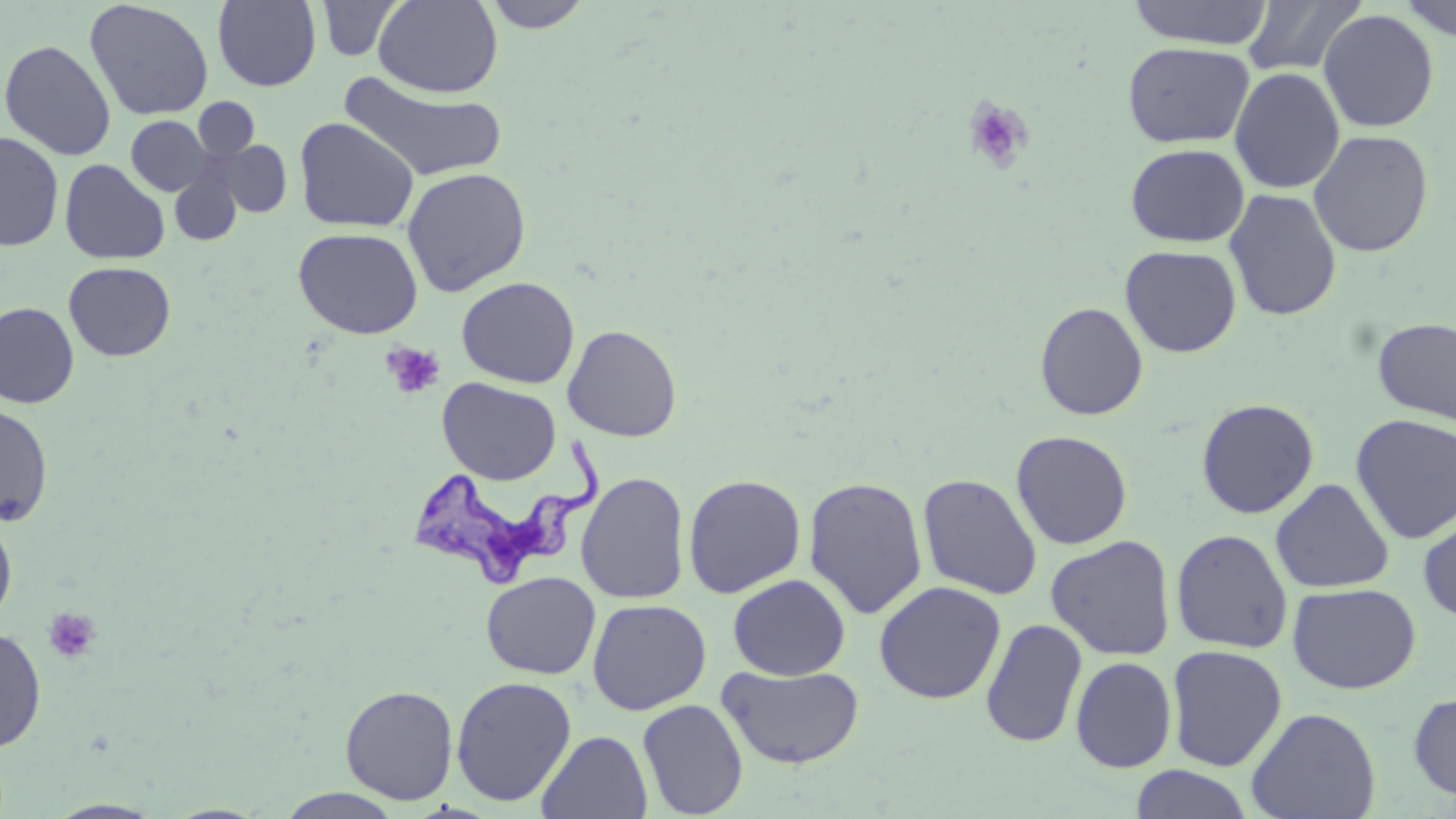

slide-level diagnosis = Trypanosoma brucei
modality = optical microscopy
platelet locations = approximate bounding boxes as [x1, y1, x2, y2] in pixels: [962, 96, 1035, 174], [380, 342, 446, 400], [43, 607, 102, 664]
magnification = 1000x
uninfected red blood cell locations = approximate bounding boxes as [x1, y1, x2, y2] in pixels: [212, 0, 322, 91], [373, 0, 503, 97], [481, 0, 594, 32], [1126, 0, 1274, 49], [1242, 0, 1367, 77], [1396, 0, 1456, 42], [84, 1, 214, 121], [316, 1, 404, 61], [1318, 9, 1439, 133], [0, 39, 116, 160], [1123, 41, 1254, 148], [1229, 67, 1345, 194], [338, 72, 507, 182], [193, 98, 259, 162], [126, 115, 212, 196], [294, 116, 419, 233], [1308, 129, 1434, 257], [0, 131, 64, 251], [214, 139, 292, 217], [1125, 143, 1249, 247], [59, 158, 170, 266], [169, 166, 243, 247], [401, 167, 532, 296], [1224, 188, 1342, 322], [293, 227, 424, 339], [1120, 245, 1242, 357], [63, 261, 176, 362], [456, 276, 580, 389], [0, 301, 80, 409], [1034, 301, 1148, 420], [1372, 317, 1456, 425], [562, 324, 682, 442], [437, 377, 561, 485], [1196, 398, 1320, 519], [0, 404, 53, 526], [1350, 414, 1456, 544], [1010, 429, 1133, 550], [575, 471, 691, 604], [917, 473, 1043, 600], [683, 474, 806, 598], [803, 476, 928, 619], [1271, 478, 1394, 594], [1417, 506, 1456, 624], [0, 511, 17, 631], [1171, 529, 1293, 653], [1046, 534, 1176, 661], [481, 571, 601, 679], [728, 574, 851, 680], [873, 581, 1007, 704], [1287, 582, 1421, 694], [587, 598, 712, 715], [980, 618, 1087, 747], [0, 626, 46, 752], [1166, 644, 1288, 771], [1070, 655, 1178, 773], [718, 664, 865, 769], [450, 676, 577, 807], [339, 685, 458, 805], [1408, 692, 1456, 801], [637, 698, 748, 818], [1246, 706, 1382, 819], [537, 730, 653, 818], [1129, 765, 1255, 819], [275, 788, 405, 818], [44, 799, 165, 818]
stain = May-Grünwald-Giemsa
field of view = one of a larger specimen
preparation = thin blood smear
image size = 1456×819 pixels
Trypanosoma brucei locations = approximate bounding boxes as [x1, y1, x2, y2] in pixels: [410, 434, 602, 589]